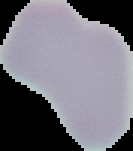
image type = segmented cell region on a black background
preparation = thin blood film
malaria status = uninfected
image size = 133×151 pixels